Identify the preparation type.
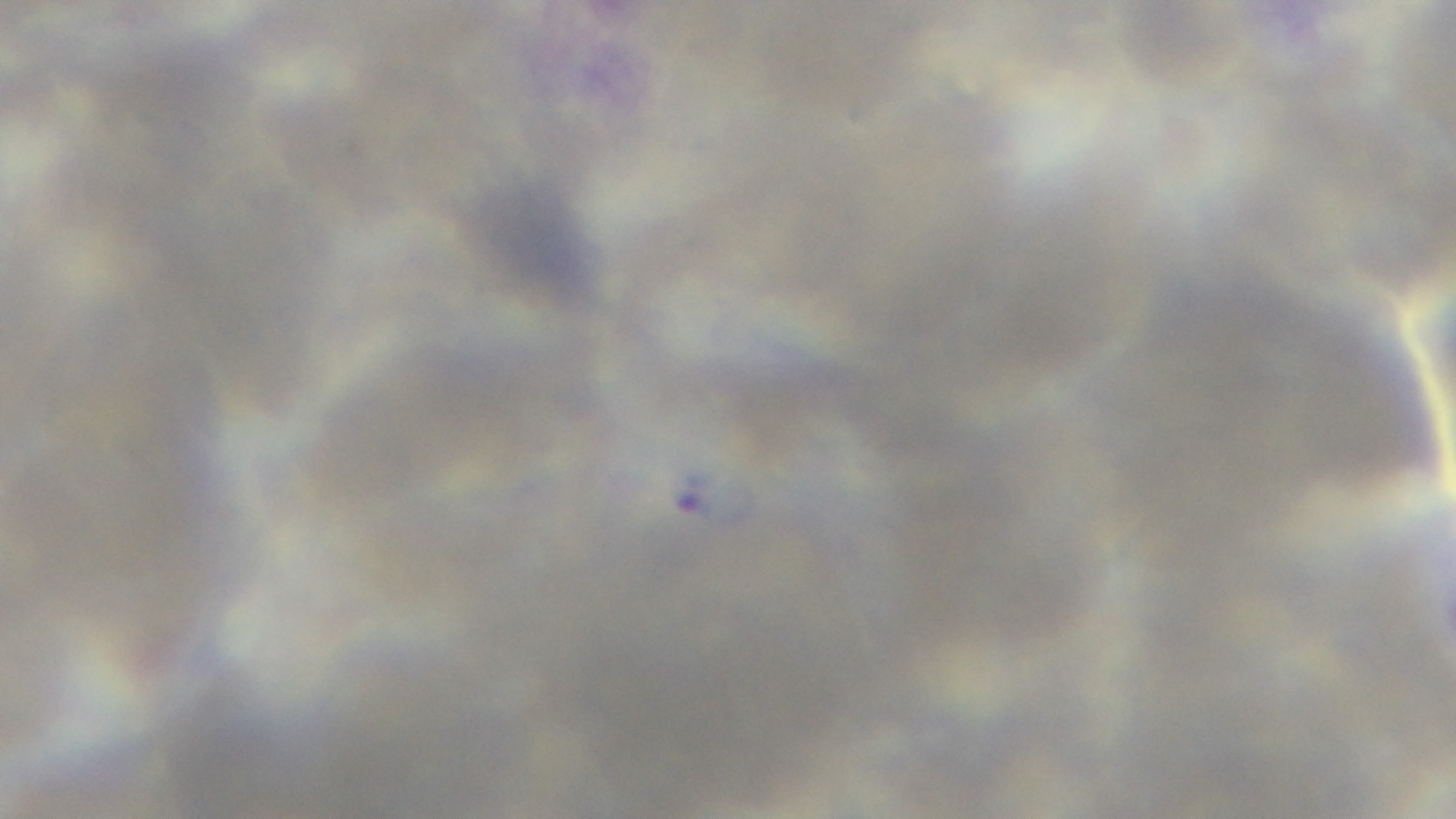
It is a thin blood film.

Summary:
  - Objective: 100x oil immersion
  - Modality: light microscopy
  - Stain: Giemsa
  - Field of view: one from the slide
  - Malaria status: positive
  - Capture: mounted 4K digital camera